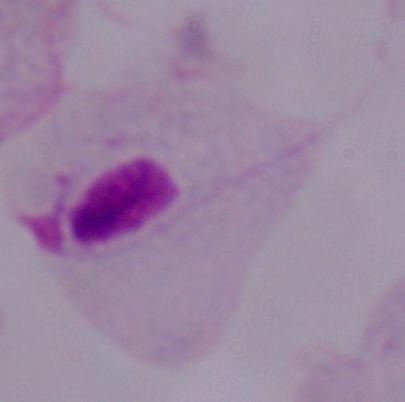
Captured at 1000x magnification. Micrograph. A trichomonad is seen.